Identify the parasite.
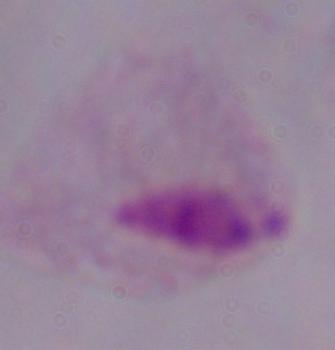
This is a trichomonad.

magnification: 1000x
modality: photomicrograph